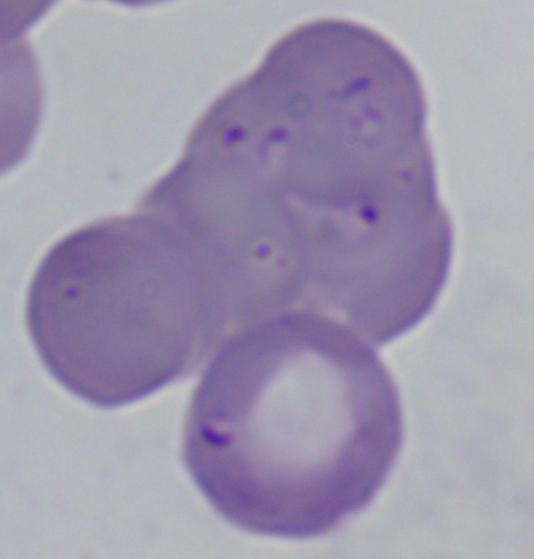

A Babesia parasite is seen. Micrograph. Captured at 1000x magnification.